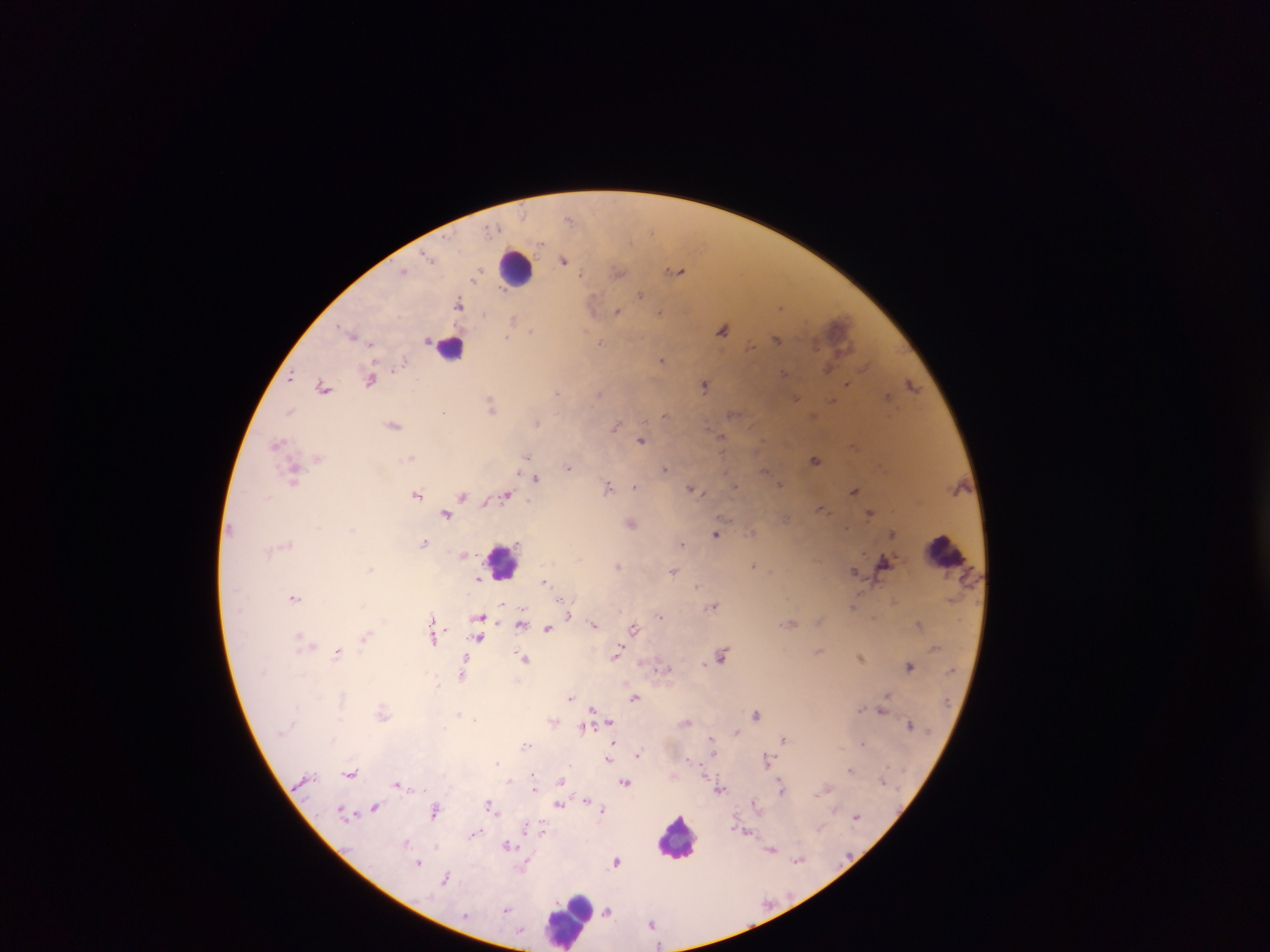 Approximate centers as [x, y] in pixels. Malaria parasite locations: [569, 219], [428, 255], [564, 259], [676, 270], [404, 271], [478, 271], [619, 273], [581, 274], [641, 294], [458, 303], [593, 303], [780, 306], [618, 311], [660, 311], [512, 320], [722, 329], [531, 331], [352, 334], [507, 338], [776, 339], [428, 340], [371, 342], [600, 343], [750, 346], [661, 360], [402, 361], [827, 369], [784, 372], [292, 377], [371, 379], [705, 384], [847, 384], [912, 385], [323, 387], [557, 393], [599, 393], [887, 397], [795, 398], [833, 400], [491, 405], [289, 411], [443, 413], [664, 414], [538, 423], [394, 425], [615, 425], [722, 436], [641, 440], [277, 443], [527, 456], [411, 457], [318, 458], [816, 460], [568, 467], [665, 469], [764, 471], [517, 472], [294, 473], [536, 479], [780, 484], [634, 486], [736, 486], [607, 487], [691, 488], [854, 491], [418, 494], [463, 495], [505, 495], [485, 504], [821, 508], [870, 513], [446, 514], [631, 523], [891, 533], [716, 534], [424, 542], [682, 543], [464, 555], [884, 561], [618, 565], [754, 565], [371, 568], [673, 571], [855, 571], [478, 578], [544, 581], [698, 587], [294, 597], [502, 604], [712, 606], [854, 606], [570, 615], [660, 616], [479, 617], [521, 623], [594, 625], [919, 625], [547, 628], [634, 628], [364, 637], [434, 638], [480, 638], [301, 639], [338, 652], [616, 654], [722, 655], [860, 657], [524, 658], [704, 664], [463, 665], [909, 666], [661, 667], [461, 674], [887, 695], [571, 698], [635, 698], [592, 708], [860, 709], [882, 710], [383, 712], [458, 715], [756, 715], [475, 720], [610, 721], [687, 722], [910, 725], [582, 728], [737, 732], [713, 738], [784, 739], [613, 742], [862, 743], [526, 745], [714, 752], [637, 755], [608, 759], [688, 759], [767, 760], [498, 763], [850, 769], [350, 773], [534, 774], [509, 781], [561, 781], [882, 781], [625, 783], [397, 784], [781, 787], [534, 789], [826, 789], [720, 790], [587, 799], [754, 802], [490, 805], [559, 805], [374, 807], [602, 809], [434, 810], [342, 811], [857, 817], [527, 827], [542, 829], [746, 833], [474, 834], [406, 841], [508, 845], [436, 846], [772, 849], [798, 860], [419, 862], [617, 862], [525, 868], [446, 878], [507, 909], [607, 911], [651, 923]. Leukocyte locations: [516, 269], [451, 346], [945, 551], [504, 560], [678, 837], [568, 919]. Image is 1270×952 pixels. Photographed through a microscope with a mobile-phone camera. Thick blood film. One field of view. Sample from Ghana.